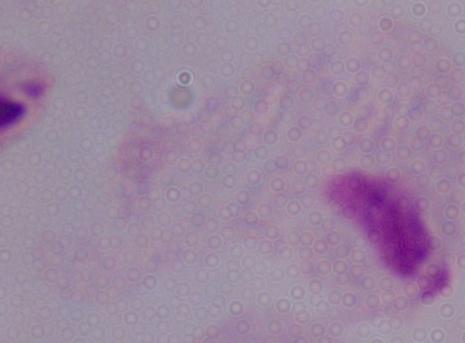

1000x magnification. Photomicrograph. A trichomonad is seen.